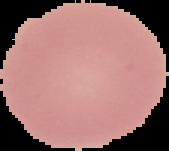
Summary:
  - Malaria status: uninfected
  - Image size: 169×151 pixels
  - Image type: segmented cell region with the area outside set to black
  - Preparation: thin blood film